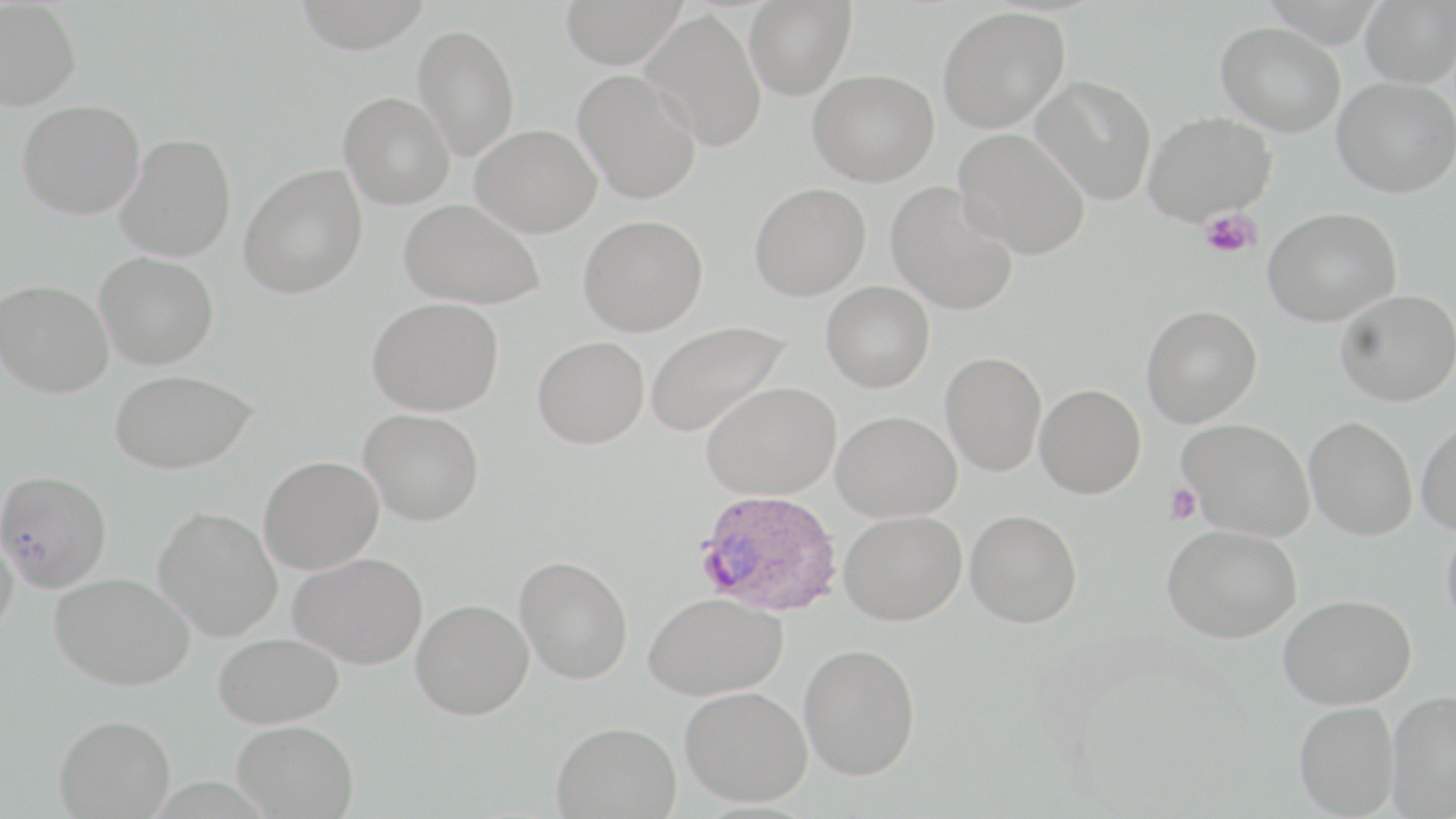
Summary:
  - Coordinate format: approximate bounding boxes as (x1, y1, x2, y2) in pixels
  - Uninfected red blood cell locations: (293, 0, 433, 53), (560, 0, 687, 69), (744, 0, 857, 100), (1360, 0, 1456, 88), (0, 1, 81, 111), (938, 6, 1070, 132), (641, 9, 766, 152), (1216, 21, 1346, 136), (412, 24, 520, 161), (572, 69, 702, 204), (808, 69, 939, 186), (1031, 75, 1157, 205), (1333, 76, 1456, 197), (338, 91, 455, 209), (17, 100, 145, 219), (1143, 112, 1275, 225), (471, 124, 601, 237), (954, 128, 1091, 259), (116, 133, 236, 262), (239, 165, 368, 299), (886, 181, 1019, 315), (750, 182, 871, 301), (399, 198, 544, 310), (1263, 207, 1402, 326), (578, 214, 708, 336), (94, 251, 218, 370), (0, 279, 113, 398), (821, 281, 935, 392), (1335, 289, 1456, 406), (367, 297, 503, 416), (1141, 304, 1262, 427), (643, 319, 790, 439), (532, 336, 649, 448), (940, 351, 1046, 476), (110, 369, 257, 474), (701, 381, 840, 500), (1034, 383, 1146, 498), (359, 409, 484, 525), (832, 410, 961, 522), (1304, 416, 1417, 540), (1177, 418, 1314, 540), (1416, 419, 1456, 534), (259, 455, 384, 573), (0, 469, 113, 593), (153, 506, 283, 642), (964, 509, 1082, 628), (839, 510, 967, 625), (1442, 517, 1456, 636), (0, 522, 19, 640), (1162, 524, 1301, 643), (289, 552, 427, 669), (514, 555, 633, 684), (50, 572, 195, 690), (644, 592, 788, 700), (1278, 594, 1416, 709), (411, 598, 534, 719), (213, 632, 345, 727), (798, 642, 921, 780), (680, 686, 812, 806), (1385, 689, 1456, 817), (1293, 701, 1400, 817), (54, 714, 175, 818), (231, 720, 359, 818), (552, 720, 681, 818)
  - Plasmodium ovale-infected red blood cell locations: (694, 489, 842, 617)
  - Platelet locations: (1199, 210, 1262, 259), (1164, 482, 1202, 524)
  - Slide-level diagnosis: Plasmodium ovale
  - Image size: 1456×819 pixels
  - Modality: light microscopy
  - Stain: May-Grünwald-Giemsa
  - Magnification: 1000x
  - Field of view: one of a larger specimen
  - Preparation: thin blood smear